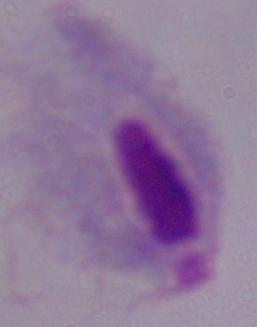
modality = micrograph
magnification = 1000x
identification = trichomonad